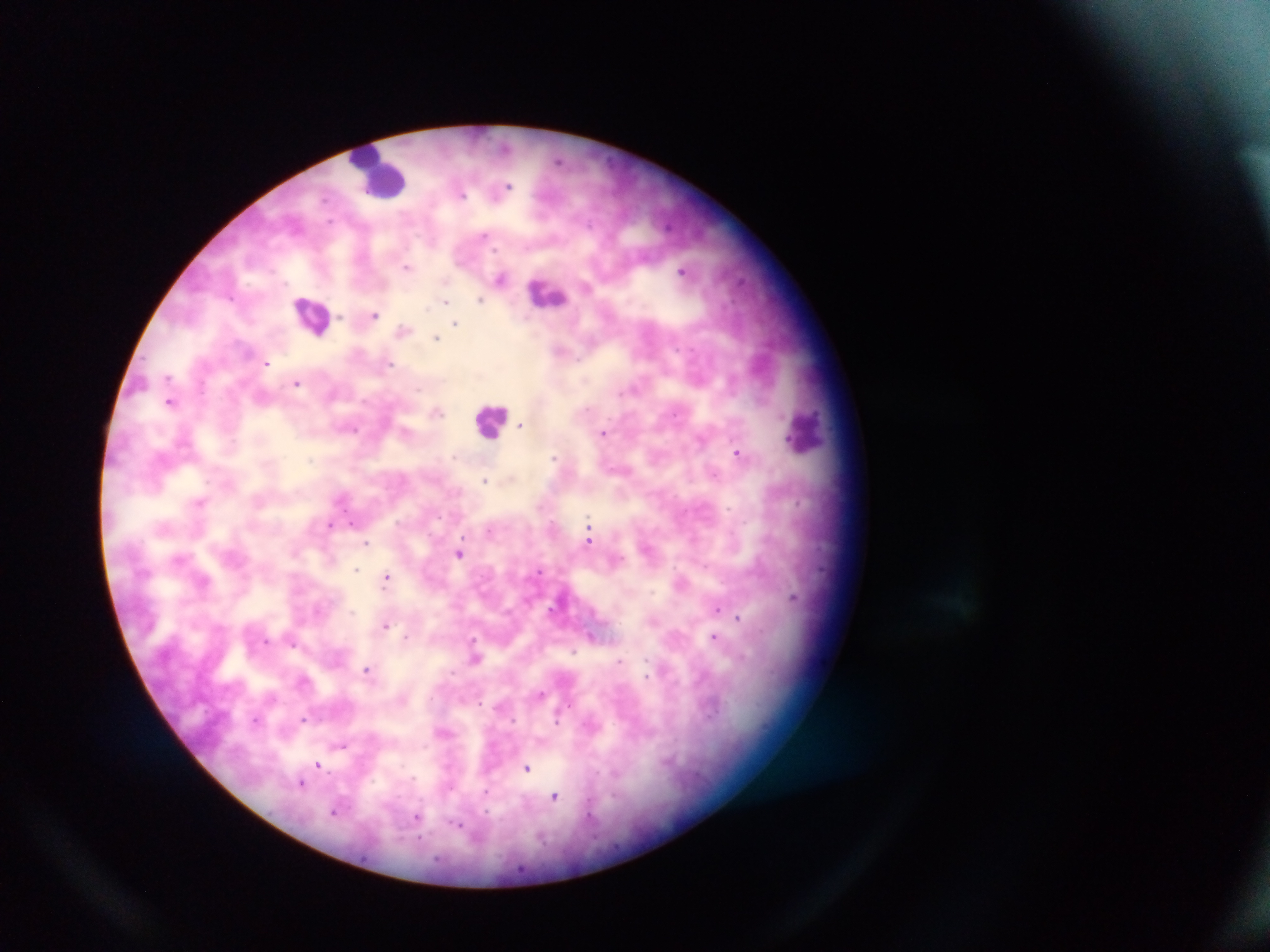

Approximate centers as [x, y] in pixels. Malaria parasite locations: [509, 184], [464, 193], [485, 232], [495, 249], [407, 267], [444, 281], [231, 299], [297, 301], [429, 306], [448, 306], [375, 313], [339, 317], [455, 321], [321, 333], [437, 338], [267, 363], [389, 366], [168, 376], [296, 385], [418, 389], [171, 402], [438, 412], [522, 423], [356, 429], [605, 433], [736, 453], [553, 456], [451, 457], [485, 481], [798, 502], [354, 523], [329, 526], [590, 534], [367, 543], [458, 553], [357, 568], [823, 568], [541, 571], [387, 576], [652, 593], [794, 601], [718, 608], [352, 613], [738, 618], [385, 625], [594, 635], [407, 636], [474, 636], [714, 637], [268, 640], [294, 645], [574, 652], [621, 662], [367, 670], [646, 674], [543, 695], [304, 718], [558, 720], [342, 745], [319, 765], [528, 768], [302, 783], [484, 794], [555, 797], [334, 813], [418, 816], [457, 827]. Leukocyte locations: [376, 173], [547, 293], [491, 422], [805, 435]. Thick blood film. Collected in Ghana. Image is 1270×952 pixels. One field of view. Mobile-phone photograph taken through the microscope.